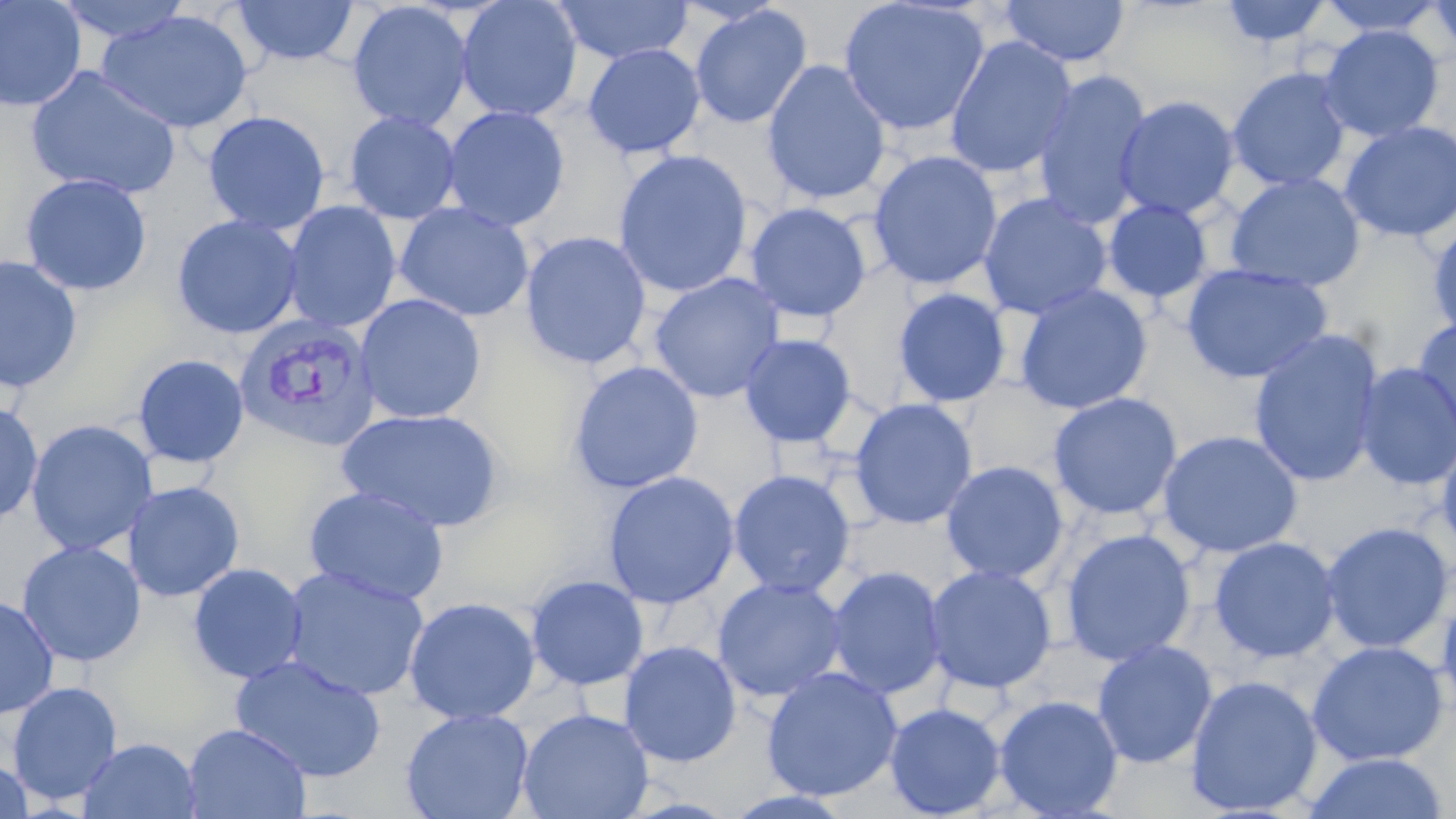

slide-level diagnosis = Plasmodium vivax
uninfected red blood cell locations = approximate bounding boxes as named x1/y1/x2/y2 corners in pixels: (x1=0, y1=0, x2=87, y2=112), (x1=53, y1=0, x2=193, y2=44), (x1=457, y1=0, x2=582, y2=122), (x1=838, y1=0, x2=991, y2=136), (x1=1001, y1=0, x2=1129, y2=68), (x1=1218, y1=0, x2=1333, y2=48), (x1=1315, y1=0, x2=1450, y2=37), (x1=1426, y1=0, x2=1456, y2=61), (x1=230, y1=1, x2=361, y2=67), (x1=347, y1=1, x2=474, y2=132), (x1=553, y1=1, x2=693, y2=64), (x1=690, y1=5, x2=811, y2=129), (x1=977, y1=6, x2=1126, y2=128), (x1=96, y1=9, x2=254, y2=134), (x1=1319, y1=24, x2=1444, y2=142), (x1=944, y1=35, x2=1078, y2=179), (x1=583, y1=44, x2=705, y2=159), (x1=762, y1=59, x2=892, y2=205), (x1=25, y1=66, x2=182, y2=200), (x1=1227, y1=66, x2=1353, y2=192), (x1=1032, y1=69, x2=1154, y2=230), (x1=1114, y1=95, x2=1240, y2=220), (x1=442, y1=106, x2=570, y2=231), (x1=203, y1=111, x2=330, y2=234), (x1=344, y1=111, x2=462, y2=224), (x1=1340, y1=119, x2=1456, y2=242), (x1=613, y1=150, x2=753, y2=298), (x1=868, y1=151, x2=1003, y2=290), (x1=1224, y1=173, x2=1366, y2=292), (x1=20, y1=174, x2=152, y2=296), (x1=978, y1=192, x2=1112, y2=320), (x1=1103, y1=199, x2=1213, y2=304), (x1=283, y1=201, x2=401, y2=332), (x1=395, y1=202, x2=535, y2=322), (x1=745, y1=202, x2=872, y2=322), (x1=172, y1=214, x2=303, y2=339), (x1=1428, y1=220, x2=1456, y2=341), (x1=520, y1=231, x2=652, y2=370), (x1=0, y1=256, x2=83, y2=394), (x1=1181, y1=263, x2=1333, y2=385), (x1=649, y1=273, x2=785, y2=403), (x1=1014, y1=284, x2=1153, y2=414), (x1=893, y1=288, x2=1012, y2=408), (x1=355, y1=294, x2=487, y2=424), (x1=1412, y1=317, x2=1456, y2=447), (x1=1248, y1=329, x2=1385, y2=487), (x1=739, y1=333, x2=857, y2=448), (x1=133, y1=354, x2=249, y2=468), (x1=567, y1=361, x2=704, y2=494), (x1=1355, y1=364, x2=1456, y2=490), (x1=1048, y1=392, x2=1183, y2=521), (x1=849, y1=398, x2=977, y2=530), (x1=0, y1=401, x2=43, y2=526), (x1=338, y1=408, x2=506, y2=533), (x1=26, y1=419, x2=158, y2=556), (x1=1157, y1=430, x2=1304, y2=559), (x1=1436, y1=433, x2=1456, y2=559), (x1=940, y1=461, x2=1069, y2=584), (x1=728, y1=470, x2=856, y2=598), (x1=602, y1=471, x2=740, y2=609), (x1=122, y1=481, x2=245, y2=602), (x1=303, y1=486, x2=450, y2=607), (x1=1320, y1=522, x2=1454, y2=654), (x1=1060, y1=528, x2=1196, y2=667), (x1=1209, y1=536, x2=1340, y2=664), (x1=17, y1=541, x2=146, y2=667), (x1=187, y1=563, x2=308, y2=684), (x1=924, y1=564, x2=1057, y2=694), (x1=281, y1=566, x2=430, y2=702), (x1=826, y1=566, x2=948, y2=699), (x1=526, y1=576, x2=649, y2=691), (x1=712, y1=577, x2=847, y2=702), (x1=1437, y1=585, x2=1456, y2=725), (x1=0, y1=596, x2=59, y2=719), (x1=403, y1=596, x2=541, y2=724), (x1=1091, y1=639, x2=1217, y2=768), (x1=619, y1=640, x2=742, y2=767), (x1=1308, y1=641, x2=1449, y2=766), (x1=230, y1=654, x2=387, y2=783), (x1=762, y1=666, x2=903, y2=802), (x1=1185, y1=674, x2=1323, y2=816), (x1=6, y1=680, x2=123, y2=806), (x1=993, y1=695, x2=1124, y2=818), (x1=884, y1=702, x2=1006, y2=817), (x1=401, y1=707, x2=534, y2=819), (x1=516, y1=708, x2=654, y2=819), (x1=183, y1=723, x2=311, y2=818), (x1=77, y1=737, x2=202, y2=819), (x1=1302, y1=752, x2=1450, y2=818), (x1=0, y1=757, x2=34, y2=818), (x1=723, y1=788, x2=857, y2=818)
stain = May-Grünwald-Giemsa
field of view = single
magnification = 1000x
image size = 1456×819 pixels
Plasmodium vivax-infected red blood cell locations = approximate bounding boxes as named x1/y1/x2/y2 corners in pixels: (x1=233, y1=314, x2=381, y2=452)
preparation = thin blood film
modality = optical microscopy